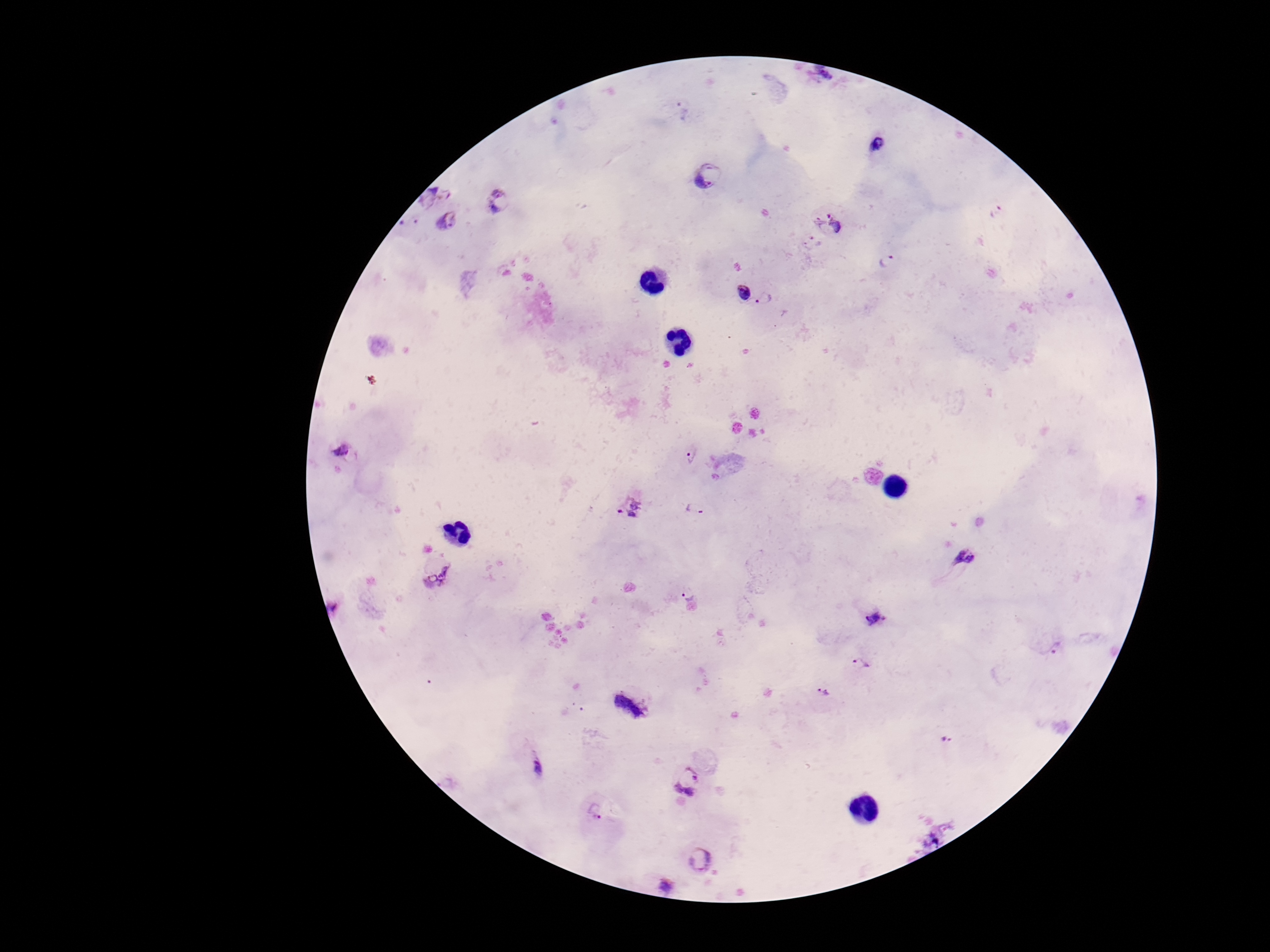
magnification: 100x
field_of_view: single
capture: smartphone camera through the microscope eyepiece
stain: Giemsa
patient_malaria_status: positive
image_size: 1270×952 pixels
plasmodium_parasite_locations: 'approximate centers as [x, y] in pixels: [881, 149], [708, 175], [498, 201], [995, 212], [447, 223], [827, 224], [811, 242], [889, 262], [742, 292], [765, 299], [342, 452], [690, 455], [631, 508], [694, 509], [965, 557], [437, 572], [688, 592], [875, 616], [1056, 644], [862, 665], [822, 691], [629, 703], [948, 737], [535, 766], [688, 779], [596, 809], [703, 856], [663, 881]'
preparation: thick blood film